State which cell type is depicted.
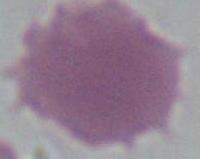
An erythrocyte.

Summary:
  - Modality: photomicrograph
  - Magnification: 1000x